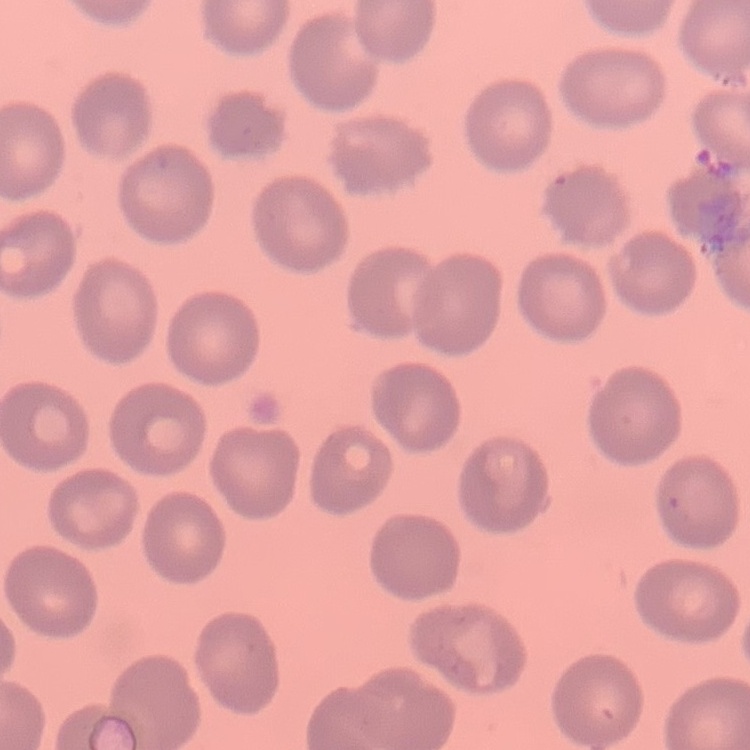
Summary:
  - Red blood cell morphology: no rouleaux formation
  - Preparation: thin blood smear
  - Stain: Field's or Giemsa
  - Image type: square crop of a larger photomicrograph